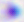

Summary:
  - Identification: Toxoplasma gondii
  - Magnification: 400x
  - Modality: photomicrograph